Locate every blood parasite and identify its species.
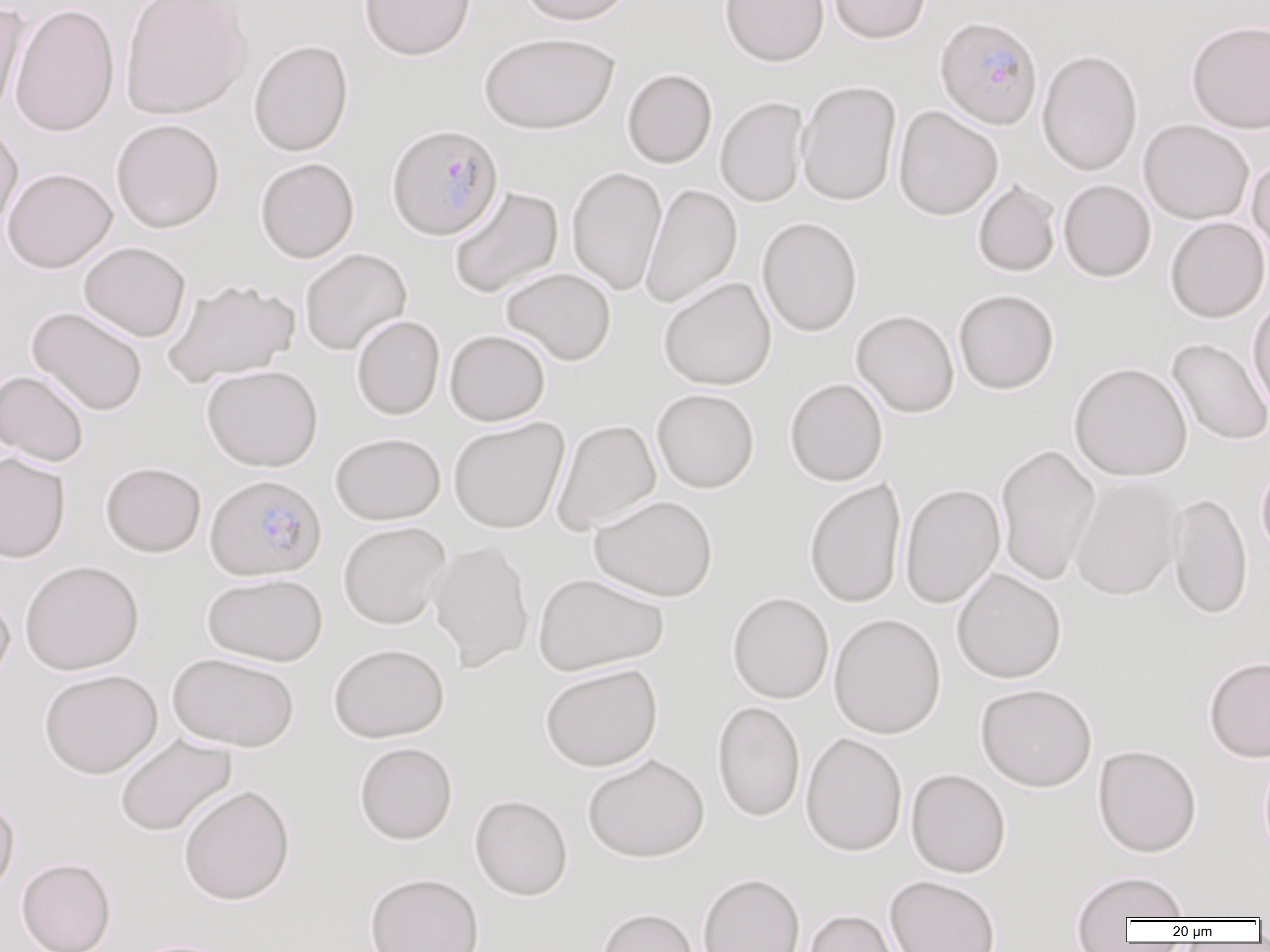

Approximate bounding boxes as named x1/y1/x2/y2 corners in pixels.
Plasmodium falciparum-infected red blood cells: (x1=935, y1=16, x2=1043, y2=130), (x1=386, y1=123, x2=504, y2=241), (x1=205, y1=473, x2=327, y2=580).
No Plasmodium ovale, Plasmodium malariae, Plasmodium vivax, Babesia divergens, or Trypanosoma brucei observed.

Uninfected red blood cell locations: (x1=120, y1=0, x2=253, y2=120), (x1=358, y1=0, x2=477, y2=61), (x1=518, y1=0, x2=636, y2=27), (x1=720, y1=0, x2=830, y2=67), (x1=828, y1=0, x2=932, y2=44), (x1=1, y1=1, x2=30, y2=118), (x1=10, y1=4, x2=120, y2=137), (x1=1186, y1=20, x2=1270, y2=134), (x1=479, y1=31, x2=619, y2=135), (x1=248, y1=39, x2=354, y2=156), (x1=1037, y1=48, x2=1143, y2=176), (x1=622, y1=69, x2=718, y2=168), (x1=796, y1=80, x2=902, y2=206), (x1=715, y1=97, x2=809, y2=207), (x1=893, y1=106, x2=1004, y2=221), (x1=110, y1=119, x2=225, y2=233), (x1=1138, y1=119, x2=1255, y2=225), (x1=0, y1=121, x2=23, y2=235), (x1=1247, y1=155, x2=1270, y2=264), (x1=255, y1=157, x2=359, y2=263), (x1=566, y1=166, x2=667, y2=296), (x1=2, y1=167, x2=117, y2=273), (x1=1058, y1=179, x2=1156, y2=282), (x1=972, y1=180, x2=1061, y2=277), (x1=640, y1=184, x2=742, y2=308), (x1=448, y1=186, x2=564, y2=299), (x1=757, y1=217, x2=862, y2=337), (x1=1165, y1=217, x2=1270, y2=323), (x1=78, y1=241, x2=191, y2=343), (x1=300, y1=248, x2=412, y2=356), (x1=501, y1=267, x2=616, y2=365), (x1=163, y1=277, x2=301, y2=387), (x1=659, y1=277, x2=776, y2=390), (x1=954, y1=289, x2=1060, y2=395), (x1=1247, y1=297, x2=1270, y2=417), (x1=26, y1=306, x2=148, y2=416), (x1=851, y1=310, x2=960, y2=418), (x1=351, y1=315, x2=445, y2=420), (x1=445, y1=329, x2=551, y2=426), (x1=1167, y1=339, x2=1270, y2=447), (x1=1069, y1=361, x2=1193, y2=481), (x1=201, y1=365, x2=323, y2=472), (x1=0, y1=369, x2=89, y2=467), (x1=784, y1=377, x2=888, y2=487), (x1=652, y1=389, x2=759, y2=493), (x1=448, y1=416, x2=570, y2=534), (x1=552, y1=419, x2=661, y2=535), (x1=330, y1=432, x2=446, y2=525), (x1=995, y1=444, x2=1101, y2=584), (x1=0, y1=453, x2=71, y2=563), (x1=1256, y1=459, x2=1270, y2=564), (x1=100, y1=461, x2=207, y2=557), (x1=1069, y1=477, x2=1183, y2=601), (x1=804, y1=478, x2=907, y2=609), (x1=899, y1=483, x2=1005, y2=609), (x1=1167, y1=493, x2=1253, y2=620), (x1=589, y1=495, x2=718, y2=601), (x1=338, y1=521, x2=451, y2=628), (x1=427, y1=541, x2=534, y2=672), (x1=19, y1=560, x2=144, y2=675), (x1=951, y1=568, x2=1067, y2=684), (x1=202, y1=573, x2=328, y2=666), (x1=533, y1=573, x2=668, y2=676), (x1=0, y1=589, x2=15, y2=688), (x1=728, y1=592, x2=833, y2=703), (x1=828, y1=613, x2=947, y2=739), (x1=328, y1=643, x2=449, y2=742), (x1=167, y1=651, x2=300, y2=752), (x1=1203, y1=657, x2=1270, y2=763), (x1=540, y1=663, x2=662, y2=772), (x1=38, y1=669, x2=163, y2=778), (x1=975, y1=683, x2=1097, y2=792), (x1=712, y1=701, x2=805, y2=822), (x1=114, y1=733, x2=237, y2=837), (x1=800, y1=733, x2=908, y2=857), (x1=354, y1=742, x2=458, y2=844), (x1=1093, y1=744, x2=1202, y2=858), (x1=1258, y1=752, x2=1270, y2=865), (x1=582, y1=754, x2=709, y2=862), (x1=905, y1=768, x2=1011, y2=878), (x1=177, y1=784, x2=296, y2=905), (x1=470, y1=794, x2=572, y2=900), (x1=0, y1=797, x2=19, y2=903), (x1=16, y1=858, x2=116, y2=952), (x1=1070, y1=870, x2=1191, y2=934), (x1=364, y1=872, x2=485, y2=952), (x1=697, y1=872, x2=806, y2=952), (x1=885, y1=875, x2=1001, y2=952), (x1=594, y1=907, x2=700, y2=952), (x1=801, y1=908, x2=905, y2=952), (x1=123, y1=938, x2=236, y2=952). Slide-level diagnosis: Plasmodium falciparum. Thin blood film. Image is 1270×952 pixels. 1000x magnification. Single field of view. Optical microscopy.